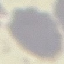

Summary:
  - Result: no malaria parasites seen
  - Image type: automatically extracted cell patch, resized to 64 × 64 pixels
  - Stain: Giemsa
  - Capture: smartphone camera at the microscope eyepiece
  - Preparation: thin blood smear